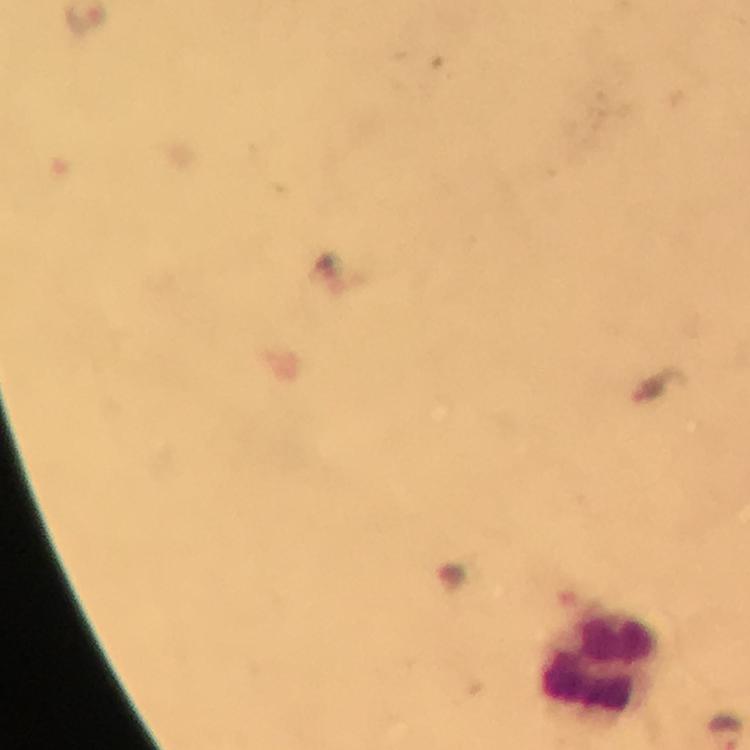
Approximate centers as {x, y} in pixels.
Summary:
  - Leukocyte locations: {601, 664}
  - Immersion oil: used
  - Image size: 750×750 pixels
  - Capture: smartphone mounted on the microscope
  - Magnification: 100x
  - Context: from a malaria diagnostic workup
  - Preparation: thick blood film
  - Plasmodium parasites: none seen
  - Stain: Giemsa
  - Cropped from: one field of view